Classify this cell by malaria status.
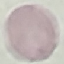

It is uninfected.

Automatically extracted cell patch, resized to 64 × 64 pixels. Thin blood smear. Giemsa-stained preparation. Photographed with a smartphone camera at the microscope eyepiece.